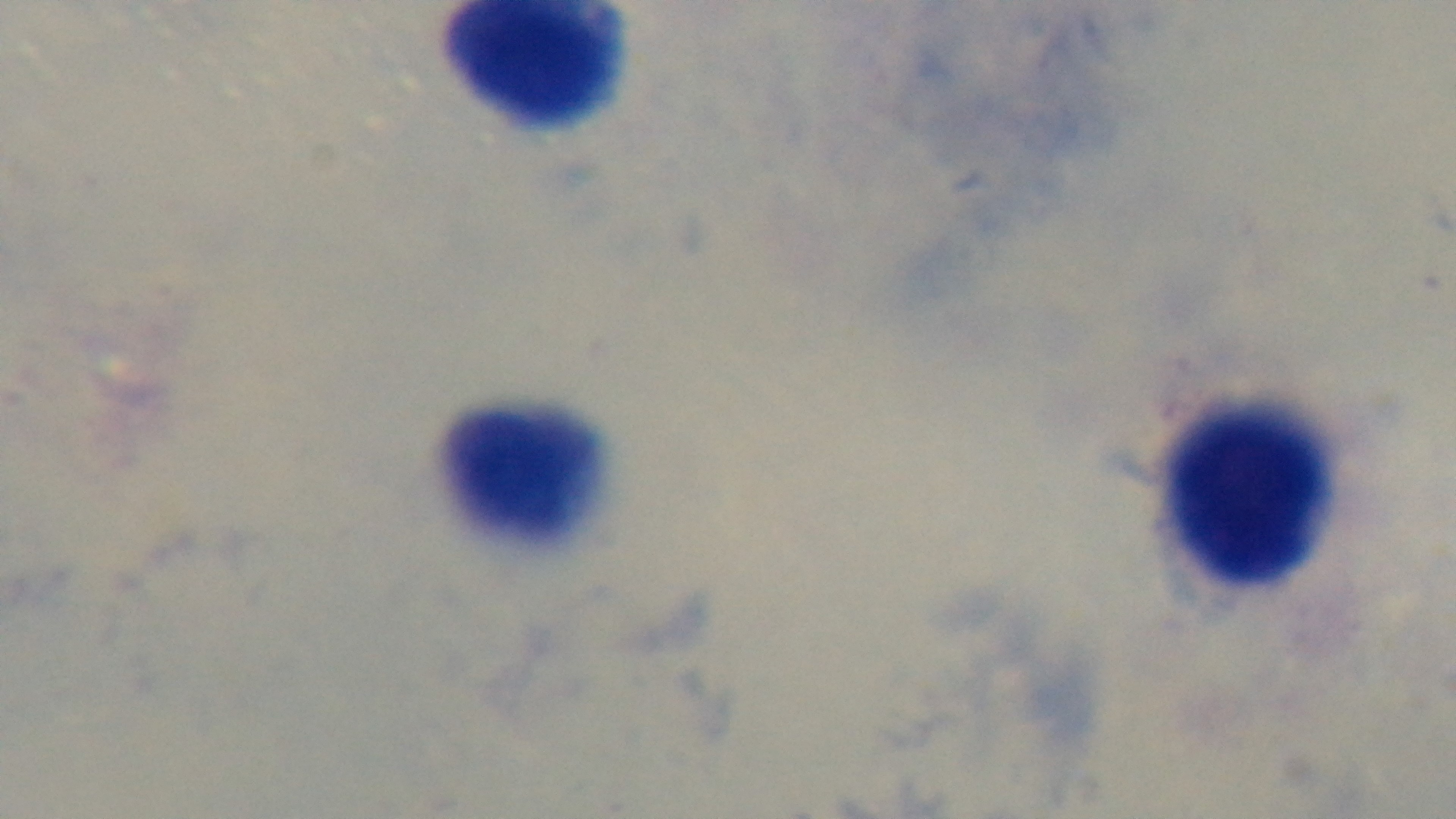
malaria status = uninfected
preparation = thick
field of view = single
modality = light microscopy
capture = mounted 4K digital camera
stain = Giemsa
objective = 100x oil immersion